Outline each blood parasite and name the species.
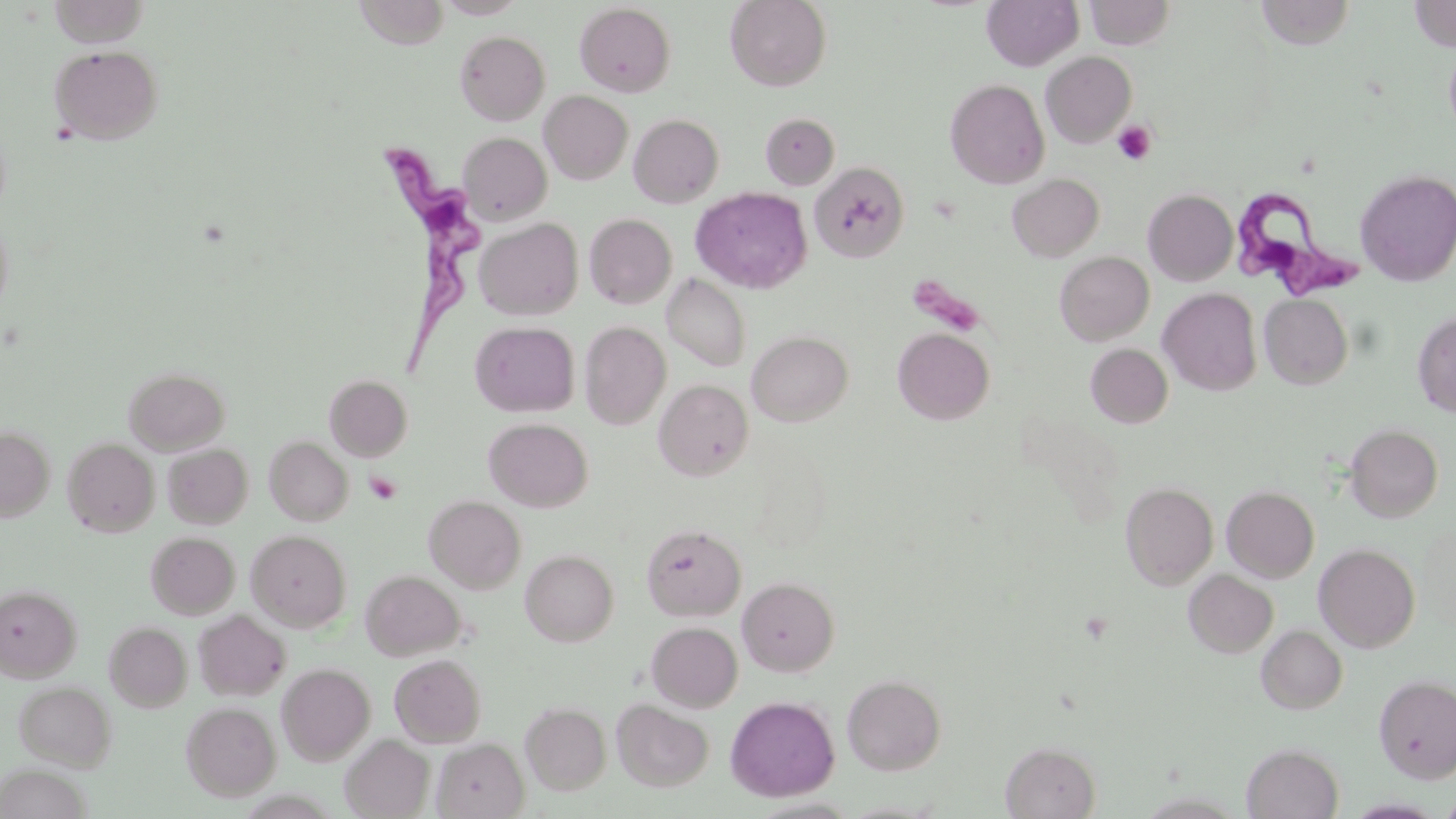

Approximate bounding boxes as [x1, y1, x2, y2] in pixels.
Trypanosoma brucei: [370, 139, 491, 377], [1227, 184, 1359, 296].
No Plasmodium falciparum, Plasmodium ovale, Plasmodium malariae, Plasmodium vivax, or Babesia divergens observed.

Summary:
  - Platelet locations: [1112, 121, 1156, 166], [364, 471, 402, 505]
  - Uninfected red blood cell locations: [353, 0, 452, 48], [435, 0, 527, 19], [725, 0, 832, 92], [982, 0, 1083, 71], [1085, 0, 1176, 50], [47, 1, 153, 47], [1254, 1, 1355, 49], [1408, 1, 1456, 52], [574, 3, 675, 97], [455, 30, 550, 125], [1444, 40, 1456, 141], [49, 45, 163, 145], [1041, 51, 1137, 147], [945, 79, 1049, 189], [540, 90, 633, 184], [760, 112, 839, 190], [629, 113, 724, 208], [458, 132, 551, 225], [810, 162, 910, 263], [1355, 170, 1456, 287], [1008, 173, 1104, 262], [691, 187, 812, 294], [1143, 189, 1238, 286], [0, 210, 15, 321], [585, 214, 676, 308], [475, 218, 582, 320], [1055, 251, 1154, 345], [662, 274, 751, 372], [1158, 287, 1262, 395], [1259, 294, 1353, 389], [1412, 311, 1456, 417], [470, 321, 580, 417], [580, 321, 671, 430], [893, 327, 994, 425], [747, 330, 853, 426], [1085, 344, 1173, 428], [124, 366, 230, 455], [325, 375, 413, 461], [654, 379, 754, 480], [484, 417, 593, 512], [1345, 424, 1443, 522], [0, 426, 55, 521], [265, 436, 353, 525], [62, 437, 159, 537], [163, 443, 253, 528], [1121, 482, 1218, 589], [1222, 485, 1320, 582], [424, 495, 526, 593], [1416, 522, 1456, 631], [641, 524, 746, 621], [246, 530, 351, 632], [146, 531, 240, 619], [1314, 543, 1420, 652], [520, 549, 618, 645], [1184, 569, 1278, 657], [361, 570, 465, 661], [737, 576, 839, 677], [1, 584, 81, 680], [194, 609, 291, 700], [105, 621, 192, 712], [646, 622, 743, 712], [1256, 624, 1347, 714], [390, 654, 486, 747], [277, 663, 375, 764], [842, 674, 946, 775], [1374, 674, 1456, 783], [13, 680, 116, 770], [725, 696, 840, 802], [611, 699, 714, 792], [181, 701, 281, 800], [521, 701, 611, 795], [340, 734, 435, 818], [433, 737, 528, 819], [1001, 741, 1101, 818], [1242, 743, 1344, 819], [0, 765, 91, 819], [1438, 793, 1456, 818]
  - Slide-level diagnosis: Trypanosoma brucei
  - Magnification: 1000x
  - Image size: 1456×819 pixels
  - Field of view: single
  - Stain: May-Grünwald-Giemsa
  - Modality: light microscopy
  - Preparation: thin blood film